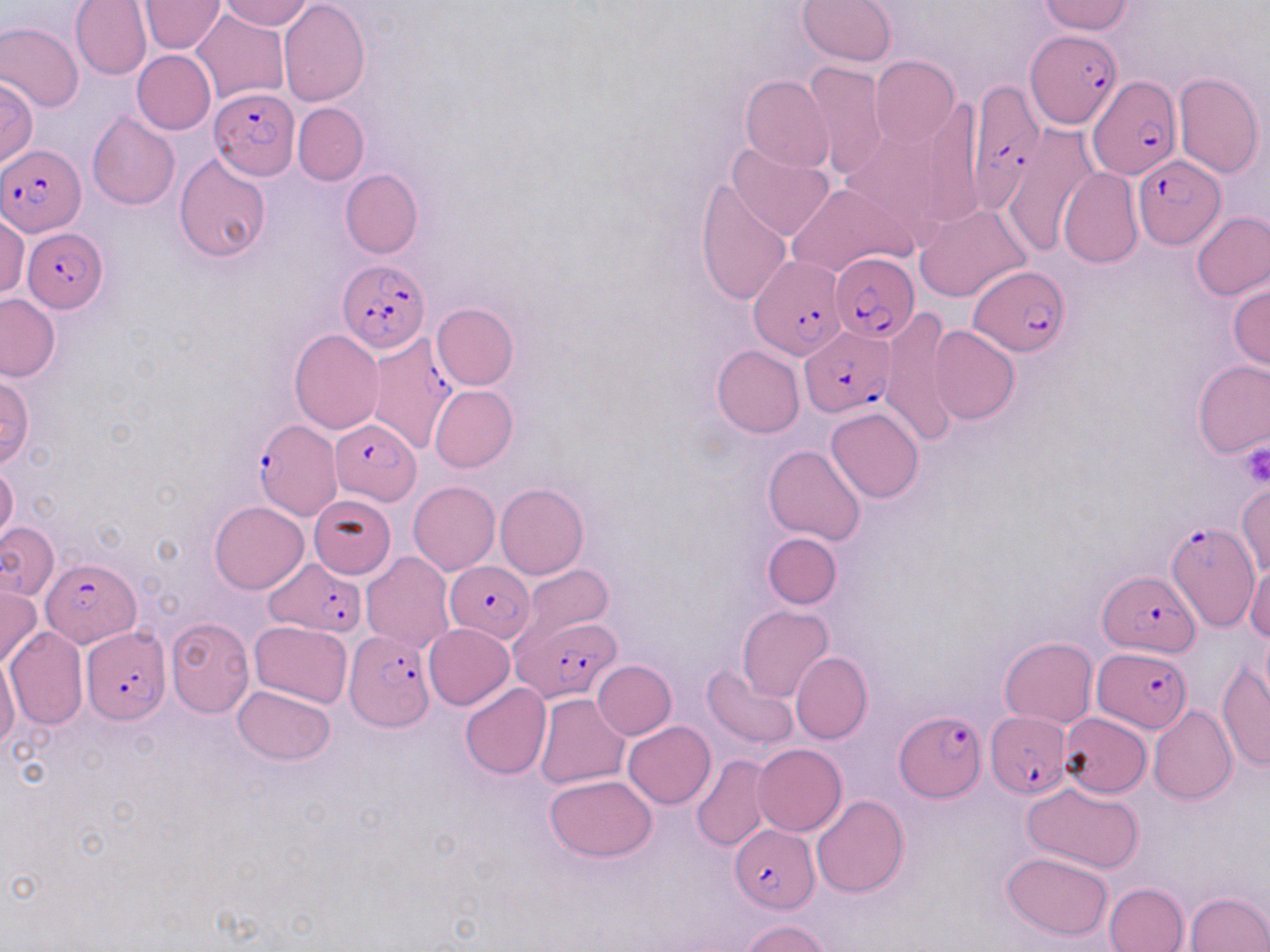
{
  "plasmodium_falciparum_infected_red_blood_cell_locations": "approximate bounding boxes as named x1/y1/x2/y2 corners in pixels: (x1=1026, y1=29, x2=1121, y2=132), (x1=1088, y1=74, x2=1182, y2=179), (x1=967, y1=85, x2=1041, y2=210), (x1=209, y1=87, x2=300, y2=179), (x1=0, y1=142, x2=87, y2=237), (x1=1133, y1=154, x2=1224, y2=249), (x1=22, y1=227, x2=109, y2=312), (x1=829, y1=253, x2=920, y2=341), (x1=750, y1=255, x2=845, y2=358), (x1=338, y1=260, x2=429, y2=354), (x1=970, y1=264, x2=1071, y2=355), (x1=800, y1=326, x2=893, y2=416), (x1=364, y1=333, x2=459, y2=454), (x1=329, y1=418, x2=420, y2=503), (x1=254, y1=420, x2=341, y2=519), (x1=1163, y1=522, x2=1259, y2=633), (x1=262, y1=555, x2=367, y2=637), (x1=41, y1=557, x2=143, y2=646), (x1=446, y1=561, x2=535, y2=642), (x1=1100, y1=574, x2=1199, y2=655), (x1=512, y1=614, x2=622, y2=701), (x1=81, y1=626, x2=173, y2=723), (x1=344, y1=628, x2=433, y2=731), (x1=1093, y1=648, x2=1193, y2=732), (x1=894, y1=710, x2=984, y2=801), (x1=986, y1=710, x2=1069, y2=797), (x1=729, y1=826, x2=818, y2=912)",
  "slide_level_diagnosis": "Plasmodium falciparum",
  "uninfected_red_blood_cell_locations": "approximate bounding boxes as named x1/y1/x2/y2 corners in pixels: (x1=70, y1=0, x2=151, y2=81), (x1=218, y1=0, x2=313, y2=29), (x1=798, y1=0, x2=895, y2=67), (x1=1036, y1=0, x2=1134, y2=35), (x1=278, y1=1, x2=369, y2=105), (x1=139, y1=2, x2=224, y2=54), (x1=190, y1=8, x2=290, y2=105), (x1=0, y1=20, x2=84, y2=113), (x1=132, y1=50, x2=215, y2=135), (x1=870, y1=55, x2=959, y2=148), (x1=803, y1=61, x2=888, y2=180), (x1=1173, y1=73, x2=1263, y2=178), (x1=741, y1=75, x2=834, y2=172), (x1=0, y1=77, x2=38, y2=166), (x1=292, y1=102, x2=369, y2=186), (x1=854, y1=102, x2=969, y2=239), (x1=88, y1=112, x2=180, y2=212), (x1=1000, y1=124, x2=1097, y2=250), (x1=726, y1=141, x2=835, y2=241), (x1=173, y1=153, x2=272, y2=263), (x1=1057, y1=168, x2=1143, y2=269), (x1=340, y1=169, x2=422, y2=259), (x1=696, y1=179, x2=794, y2=305), (x1=785, y1=182, x2=917, y2=277), (x1=915, y1=203, x2=1032, y2=302), (x1=1, y1=213, x2=29, y2=299), (x1=1192, y1=213, x2=1270, y2=299), (x1=1229, y1=281, x2=1270, y2=371), (x1=0, y1=294, x2=61, y2=382), (x1=431, y1=302, x2=518, y2=390), (x1=878, y1=311, x2=958, y2=444), (x1=929, y1=326, x2=1020, y2=425), (x1=289, y1=329, x2=383, y2=434), (x1=711, y1=345, x2=805, y2=438), (x1=1193, y1=361, x2=1269, y2=458), (x1=0, y1=374, x2=34, y2=467), (x1=429, y1=386, x2=516, y2=472), (x1=826, y1=407, x2=924, y2=503), (x1=764, y1=444, x2=868, y2=546), (x1=0, y1=464, x2=19, y2=548), (x1=409, y1=481, x2=501, y2=575), (x1=1237, y1=482, x2=1269, y2=577), (x1=495, y1=484, x2=589, y2=579), (x1=308, y1=494, x2=396, y2=578), (x1=209, y1=501, x2=308, y2=595), (x1=0, y1=521, x2=59, y2=600), (x1=762, y1=532, x2=841, y2=609), (x1=360, y1=552, x2=455, y2=654), (x1=1244, y1=560, x2=1270, y2=642), (x1=516, y1=563, x2=613, y2=647), (x1=0, y1=584, x2=42, y2=670), (x1=738, y1=606, x2=834, y2=703), (x1=165, y1=617, x2=254, y2=717), (x1=250, y1=621, x2=352, y2=707), (x1=424, y1=623, x2=515, y2=709), (x1=5, y1=627, x2=87, y2=730), (x1=999, y1=636, x2=1097, y2=727), (x1=791, y1=651, x2=871, y2=743), (x1=0, y1=657, x2=21, y2=751), (x1=592, y1=660, x2=676, y2=740), (x1=1216, y1=662, x2=1269, y2=771), (x1=702, y1=664, x2=799, y2=752), (x1=461, y1=683, x2=551, y2=779), (x1=231, y1=685, x2=336, y2=765), (x1=535, y1=693, x2=629, y2=788), (x1=1149, y1=706, x2=1238, y2=804), (x1=1059, y1=713, x2=1152, y2=797), (x1=624, y1=721, x2=716, y2=809), (x1=753, y1=744, x2=846, y2=836), (x1=691, y1=752, x2=774, y2=852), (x1=544, y1=775, x2=656, y2=861), (x1=1022, y1=781, x2=1144, y2=873), (x1=813, y1=795, x2=909, y2=897), (x1=1001, y1=851, x2=1113, y2=941), (x1=1105, y1=881, x2=1189, y2=952), (x1=1186, y1=892, x2=1270, y2=952), (x1=742, y1=919, x2=831, y2=952)",
  "field_of_view": "one of a larger specimen",
  "preparation": "thin blood film",
  "image_size": "1270×952 pixels",
  "modality": "optical microscopy",
  "magnification": "1000x",
  "stain": "May-Grünwald-Giemsa",
  "platelet_locations": "approximate bounding boxes as named x1/y1/x2/y2 corners in pixels: (x1=1240, y1=441, x2=1270, y2=486)"
}